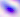 Toxoplasma gondii is seen. Captured at 400x magnification. Photomicrograph.